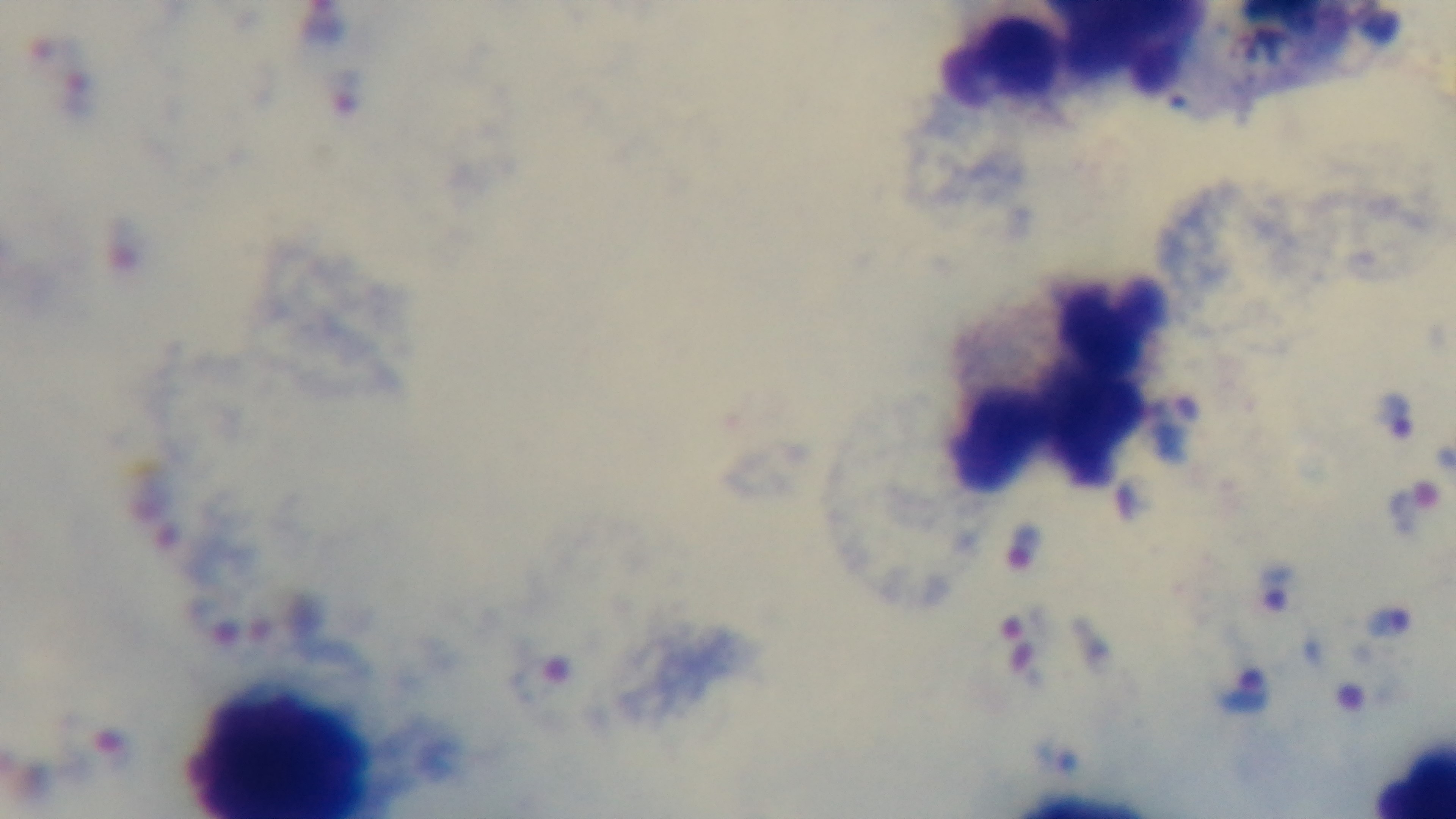
Summary:
  - Preparation: thick smear
  - Capture: mounted 4K digital camera
  - Field of view: one from the slide
  - Stain: Giemsa
  - Objective: 100x oil immersion
  - Malaria status: positive
  - Modality: light microscopy